State the blood parasite species.
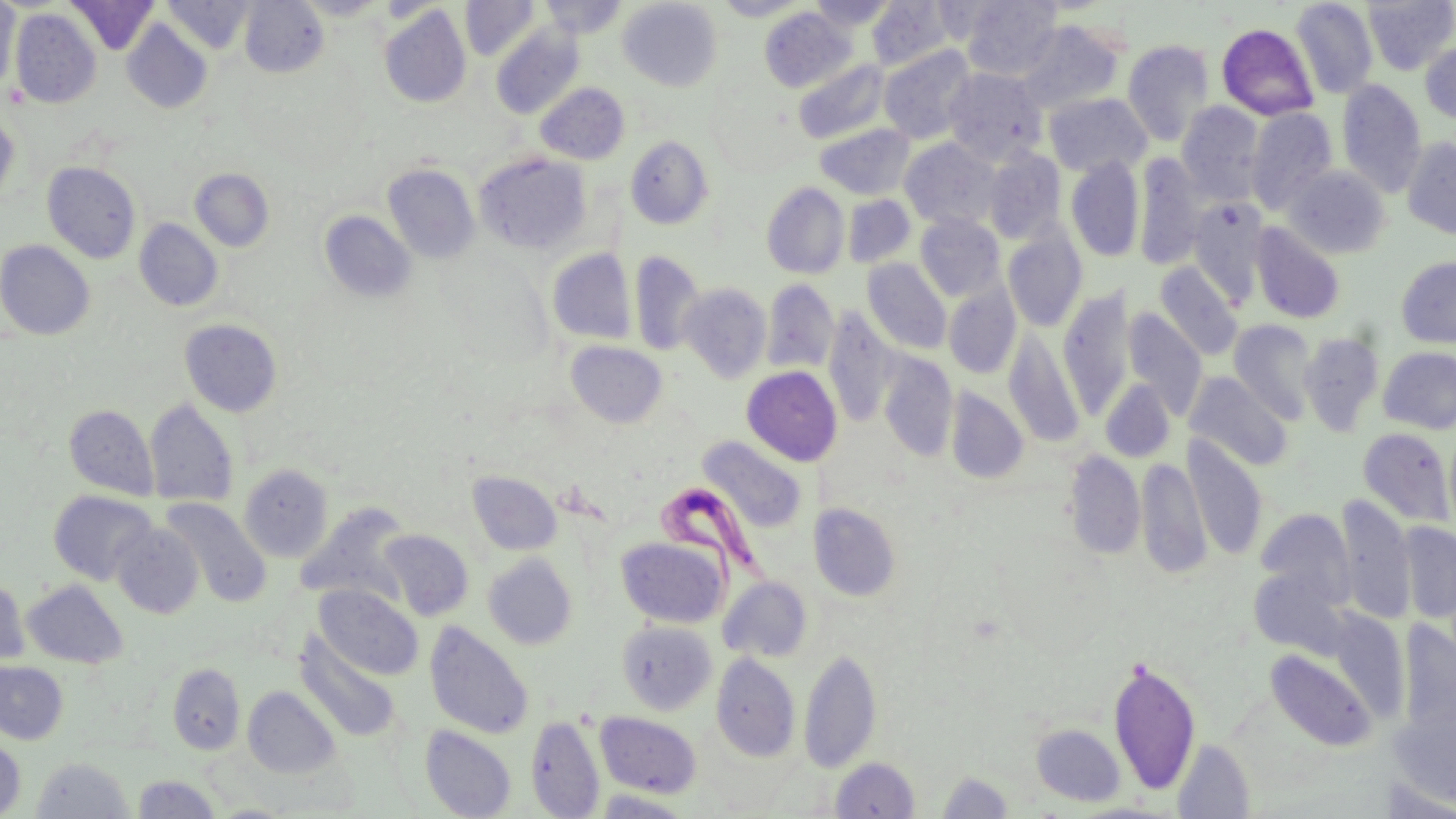

Trypanosoma brucei.

Approximate bounding boxes as (x1,y1)-(x2,y2) corner pairs in pixels. Uninfected red blood cell locations: (0,0)-(20,95), (66,0)-(159,55), (162,0)-(254,55), (239,0)-(329,77), (295,0)-(388,19), (539,0)-(628,39), (618,0)-(722,91), (713,0)-(810,20), (808,0)-(896,31), (961,0)-(1062,81), (1362,0)-(1456,75), (460,1)-(540,61), (867,1)-(954,70), (1290,1)-(1378,99), (379,5)-(471,108), (759,8)-(856,93), (10,9)-(101,108), (122,20)-(212,113), (1016,20)-(1125,114), (1216,23)-(1319,120), (491,25)-(584,120), (1122,39)-(1214,147), (1420,42)-(1456,124), (879,45)-(977,144), (794,59)-(890,144), (943,68)-(1046,165), (1336,80)-(1427,197), (536,83)-(630,164), (1044,92)-(1152,177), (1177,101)-(1265,202), (1246,108)-(1338,215), (0,113)-(19,207), (814,124)-(914,200), (625,136)-(714,229), (900,137)-(1001,231), (1402,137)-(1456,239), (983,150)-(1065,244), (475,152)-(591,254), (1133,154)-(1204,270), (1065,155)-(1144,262), (42,161)-(141,263), (383,164)-(479,263), (1284,165)-(1391,259), (190,168)-(274,252), (761,183)-(850,279), (842,194)-(914,268), (1189,198)-(1268,307), (319,210)-(416,303), (915,214)-(1005,300), (134,219)-(223,312), (1251,222)-(1346,324), (1002,226)-(1087,332), (0,239)-(95,340), (547,249)-(636,344), (629,251)-(705,356), (1396,256)-(1456,348), (862,258)-(951,355), (1154,261)-(1244,360), (762,279)-(839,374), (679,283)-(771,383), (943,283)-(1021,379), (1057,287)-(1135,416), (822,308)-(899,427), (1122,308)-(1207,419), (180,319)-(283,418), (1228,320)-(1318,424), (1005,330)-(1085,447), (1299,332)-(1384,435), (566,341)-(667,428), (1377,346)-(1456,434), (878,352)-(958,462), (742,366)-(842,466), (1185,371)-(1293,472), (1100,378)-(1176,462), (946,387)-(1028,483), (145,398)-(239,507), (64,404)-(158,499), (1358,428)-(1454,526), (697,436)-(808,535), (1182,436)-(1268,559), (1063,450)-(1145,560), (1135,457)-(1210,578), (239,464)-(333,562), (468,471)-(563,556), (48,491)-(157,585), (1336,495)-(1416,624), (161,498)-(271,607), (296,502)-(413,605), (809,503)-(901,601), (1256,509)-(1355,606), (111,523)-(204,618), (1399,523)-(1456,623), (380,529)-(474,621), (616,536)-(729,628), (483,553)-(578,650), (1249,566)-(1350,658), (0,576)-(30,666), (718,576)-(813,663), (22,580)-(128,668), (314,585)-(422,680), (425,621)-(534,739), (617,621)-(716,714), (1398,621)-(1455,741), (295,632)-(401,743), (799,648)-(882,774), (1265,649)-(1377,751), (710,653)-(800,762), (1108,657)-(1201,795), (0,661)-(68,745), (167,663)-(246,755), (243,686)-(340,779), (1390,704)-(1456,811), (595,711)-(702,798), (527,715)-(604,818), (1031,723)-(1126,806), (420,725)-(517,819), (0,735)-(27,818), (1172,738)-(1256,818), (31,756)-(134,818), (830,758)-(920,818), (935,771)-(1015,818), (131,774)-(222,817), (591,790)-(696,818). Trypanosoma brucei locations: (654,479)-(772,616). May-Grünwald-Giemsa-stained preparation. Single field of view. Light microscopy. Captured at 1000x magnification. Thin blood smear. Image is 1456×819 pixels.